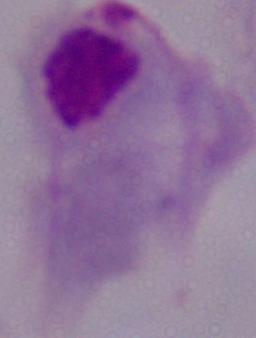
A trichomonad is seen. Captured at 1000x magnification. Micrograph.